Describe the morphology of the erythrocytes.
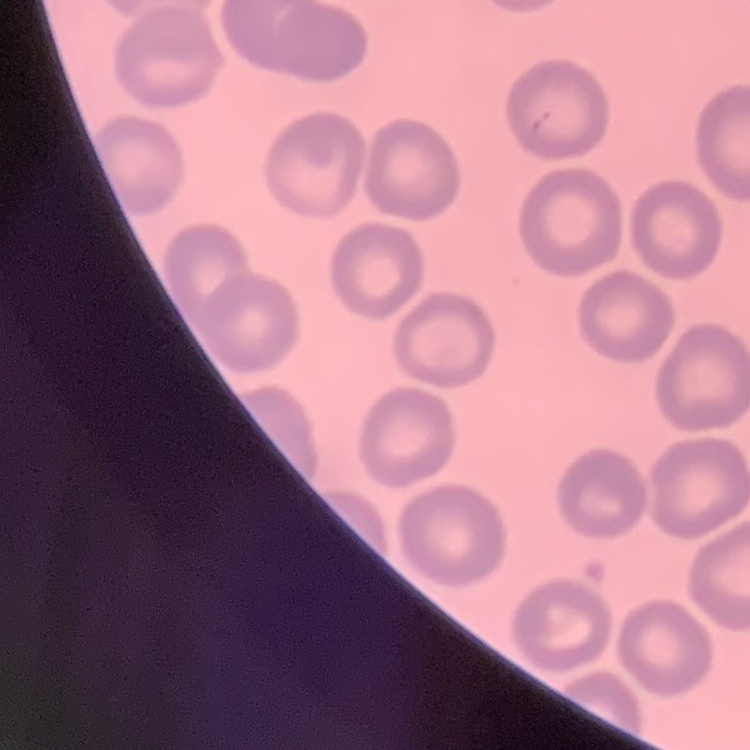
No rouleaux formation.

Square crop of a larger photomicrograph. Thin blood film. Stained with either Field's or Giemsa.